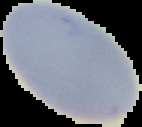
image type = segmented cell region with the area outside set to black
preparation = thin blood smear
image size = 142×127 pixels
malaria status = uninfected